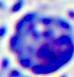
identification = leukocyte
magnification = 400x
modality = micrograph